Locate and identify every blood parasite.
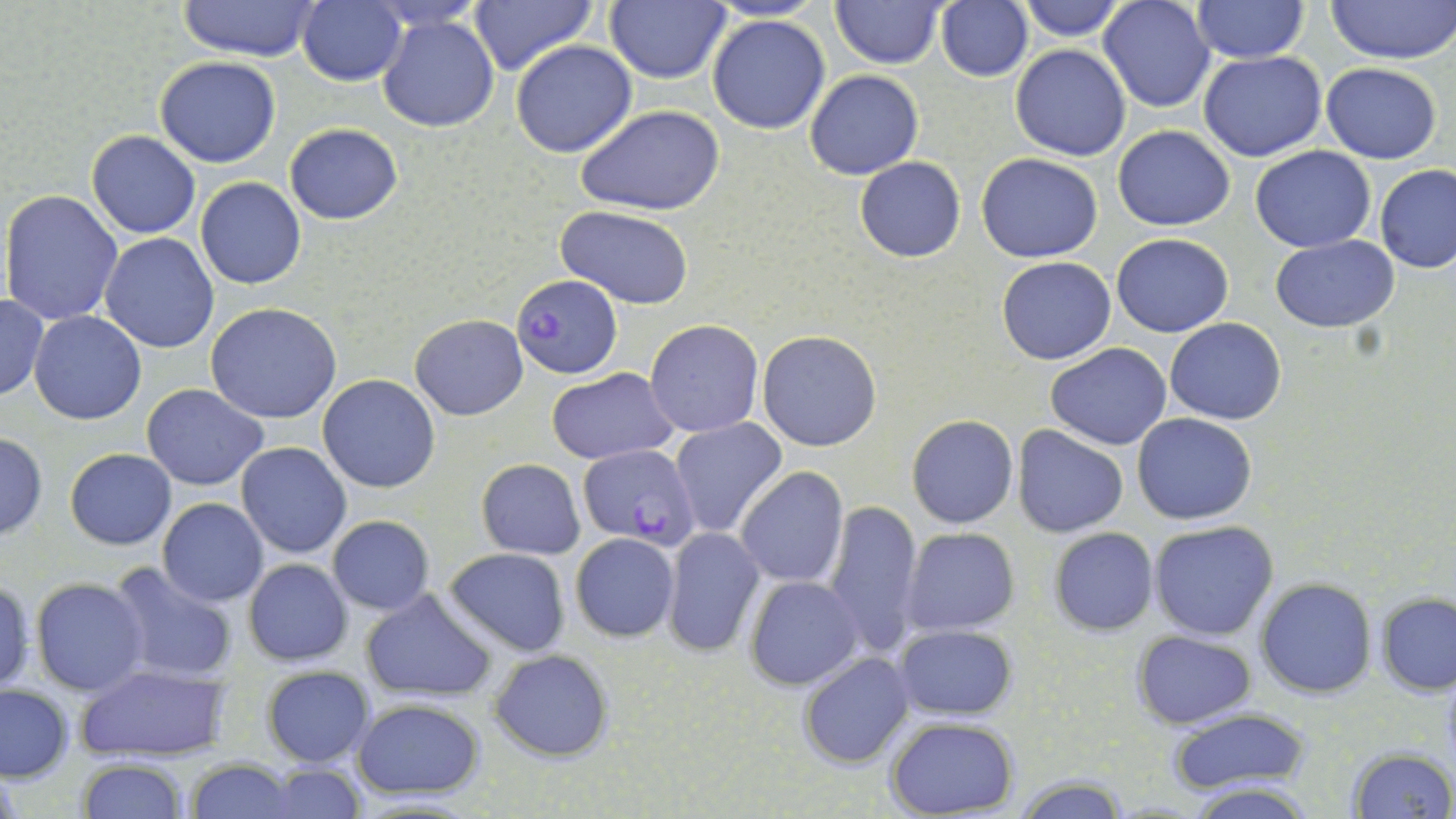
Approximate bounding boxes as named x1/y1/x2/y2 corners in pixels.
Plasmodium falciparum-infected red blood cells: (x1=511, y1=273, x2=623, y2=379), (x1=578, y1=444, x2=701, y2=549).
No Plasmodium ovale, Plasmodium malariae, Plasmodium vivax, Babesia divergens, or Trypanosoma brucei observed.

{
  "slide_level_diagnosis": "Plasmodium falciparum",
  "preparation": "thin blood film",
  "magnification": "1000x",
  "image_size": "1456×819 pixels",
  "modality": "light microscopy",
  "stain": "May-Grünwald-Giemsa",
  "field_of_view": "one of a larger specimen",
  "uninfected_red_blood_cell_locations": "approximate bounding boxes as named x1/y1/x2/y2 corners in pixels: (x1=176, y1=0, x2=321, y2=63), (x1=829, y1=0, x2=946, y2=68), (x1=1015, y1=0, x2=1129, y2=41), (x1=1191, y1=0, x2=1309, y2=65), (x1=1328, y1=0, x2=1456, y2=66), (x1=469, y1=1, x2=596, y2=76), (x1=604, y1=1, x2=731, y2=84), (x1=935, y1=1, x2=1033, y2=83), (x1=1097, y1=1, x2=1215, y2=113), (x1=296, y1=2, x2=407, y2=86), (x1=376, y1=14, x2=501, y2=134), (x1=706, y1=14, x2=832, y2=135), (x1=510, y1=38, x2=638, y2=157), (x1=1010, y1=45, x2=1131, y2=160), (x1=1198, y1=50, x2=1328, y2=162), (x1=154, y1=57, x2=281, y2=168), (x1=1320, y1=63, x2=1442, y2=164), (x1=805, y1=69, x2=924, y2=180), (x1=576, y1=103, x2=725, y2=216), (x1=285, y1=123, x2=403, y2=225), (x1=1113, y1=126, x2=1235, y2=230), (x1=85, y1=131, x2=200, y2=238), (x1=1250, y1=145, x2=1377, y2=252), (x1=976, y1=152, x2=1103, y2=263), (x1=855, y1=157, x2=966, y2=262), (x1=1374, y1=164, x2=1455, y2=274), (x1=195, y1=176, x2=307, y2=289), (x1=2, y1=189, x2=124, y2=327), (x1=556, y1=207, x2=696, y2=311), (x1=100, y1=232, x2=218, y2=354), (x1=1113, y1=234, x2=1234, y2=337), (x1=1271, y1=235, x2=1399, y2=331), (x1=996, y1=257, x2=1117, y2=366), (x1=0, y1=294, x2=48, y2=400), (x1=206, y1=303, x2=343, y2=423), (x1=30, y1=312, x2=146, y2=425), (x1=410, y1=314, x2=527, y2=420), (x1=644, y1=318, x2=764, y2=437), (x1=1165, y1=318, x2=1286, y2=424), (x1=757, y1=330, x2=883, y2=452), (x1=1047, y1=344, x2=1171, y2=449), (x1=546, y1=366, x2=679, y2=464), (x1=319, y1=374, x2=439, y2=493), (x1=142, y1=384, x2=269, y2=490), (x1=1133, y1=413, x2=1258, y2=525), (x1=669, y1=415, x2=788, y2=539), (x1=907, y1=416, x2=1017, y2=528), (x1=1012, y1=425, x2=1128, y2=537), (x1=0, y1=434, x2=49, y2=540), (x1=236, y1=441, x2=352, y2=559), (x1=64, y1=448, x2=177, y2=549), (x1=476, y1=458, x2=586, y2=559), (x1=736, y1=466, x2=849, y2=588), (x1=157, y1=498, x2=269, y2=605), (x1=823, y1=500, x2=926, y2=657), (x1=327, y1=516, x2=434, y2=616), (x1=1151, y1=521, x2=1277, y2=641), (x1=901, y1=526, x2=1022, y2=636), (x1=663, y1=527, x2=765, y2=656), (x1=1048, y1=527, x2=1159, y2=635), (x1=570, y1=532, x2=680, y2=642), (x1=442, y1=547, x2=571, y2=658), (x1=243, y1=559, x2=353, y2=666), (x1=107, y1=560, x2=238, y2=685), (x1=31, y1=576, x2=152, y2=697), (x1=744, y1=576, x2=863, y2=690), (x1=1255, y1=577, x2=1376, y2=698), (x1=0, y1=578, x2=35, y2=695), (x1=359, y1=588, x2=498, y2=701), (x1=1376, y1=591, x2=1456, y2=696), (x1=894, y1=623, x2=1020, y2=720), (x1=1132, y1=630, x2=1257, y2=727), (x1=488, y1=648, x2=615, y2=762), (x1=799, y1=652, x2=916, y2=768), (x1=74, y1=665, x2=233, y2=762), (x1=260, y1=666, x2=374, y2=766), (x1=0, y1=683, x2=74, y2=783), (x1=353, y1=697, x2=486, y2=802), (x1=1167, y1=707, x2=1314, y2=795), (x1=885, y1=716, x2=1021, y2=818), (x1=1344, y1=746, x2=1454, y2=819), (x1=77, y1=760, x2=190, y2=818), (x1=185, y1=760, x2=296, y2=818), (x1=251, y1=762, x2=371, y2=819), (x1=1012, y1=777, x2=1131, y2=817), (x1=1185, y1=783, x2=1317, y2=817)"
}